Outline each uninfected red blood cell.
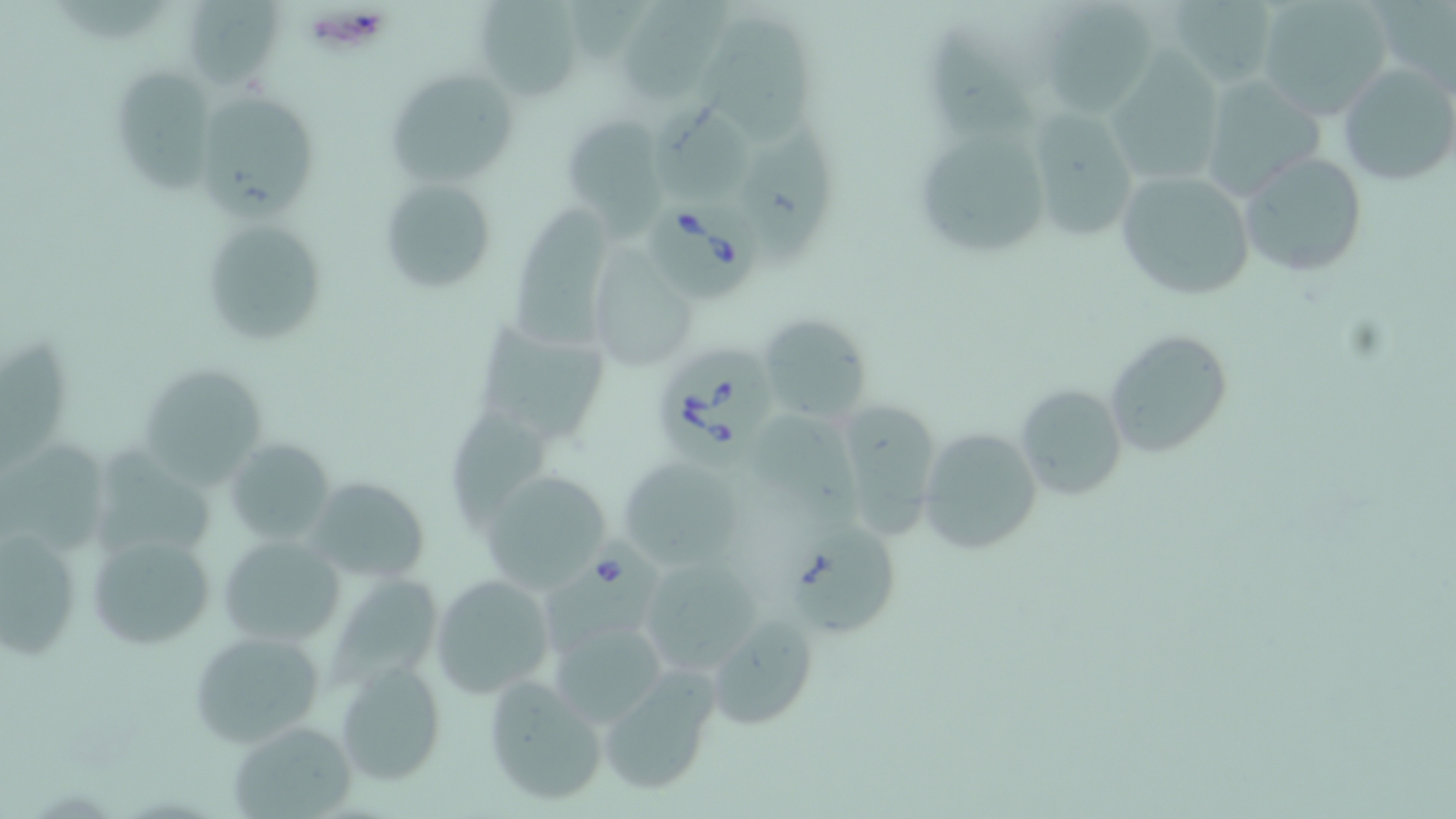

Approximate bounding boxes as named x1/y1/x2/y2 corners in pixels.
Uninfected red blood cells: (x1=54, y1=0, x2=173, y2=47), (x1=179, y1=0, x2=286, y2=91), (x1=474, y1=0, x2=585, y2=99), (x1=1162, y1=0, x2=1282, y2=90), (x1=1253, y1=0, x2=1397, y2=119), (x1=1370, y1=0, x2=1456, y2=95), (x1=611, y1=1, x2=733, y2=104), (x1=1035, y1=6, x2=1158, y2=114), (x1=693, y1=14, x2=816, y2=150), (x1=928, y1=34, x2=1033, y2=139), (x1=1103, y1=60, x2=1227, y2=188), (x1=109, y1=63, x2=219, y2=192), (x1=1338, y1=64, x2=1455, y2=188), (x1=386, y1=67, x2=520, y2=191), (x1=1197, y1=75, x2=1325, y2=199), (x1=196, y1=91, x2=320, y2=219), (x1=649, y1=94, x2=759, y2=208), (x1=1023, y1=108, x2=1138, y2=241), (x1=560, y1=114, x2=664, y2=221), (x1=923, y1=124, x2=1056, y2=253), (x1=736, y1=127, x2=840, y2=270), (x1=1237, y1=152, x2=1368, y2=277), (x1=1115, y1=169, x2=1257, y2=303), (x1=377, y1=176, x2=499, y2=294), (x1=509, y1=198, x2=624, y2=355), (x1=199, y1=215, x2=327, y2=345), (x1=587, y1=252, x2=697, y2=373), (x1=757, y1=313, x2=874, y2=422), (x1=473, y1=317, x2=612, y2=447), (x1=1104, y1=329, x2=1235, y2=459), (x1=1, y1=330, x2=75, y2=465), (x1=134, y1=363, x2=269, y2=488), (x1=1015, y1=384, x2=1128, y2=499), (x1=826, y1=399, x2=945, y2=538), (x1=449, y1=411, x2=555, y2=529), (x1=758, y1=413, x2=864, y2=528), (x1=917, y1=428, x2=1042, y2=555), (x1=225, y1=437, x2=336, y2=548), (x1=0, y1=439, x2=108, y2=567), (x1=88, y1=440, x2=223, y2=555), (x1=616, y1=455, x2=743, y2=568), (x1=477, y1=471, x2=615, y2=592), (x1=306, y1=475, x2=433, y2=583), (x1=788, y1=521, x2=899, y2=638), (x1=2, y1=529, x2=83, y2=662), (x1=85, y1=531, x2=219, y2=652), (x1=218, y1=534, x2=346, y2=648), (x1=636, y1=555, x2=770, y2=676), (x1=431, y1=574, x2=554, y2=699), (x1=328, y1=580, x2=445, y2=696), (x1=708, y1=616, x2=821, y2=730), (x1=549, y1=619, x2=665, y2=728), (x1=187, y1=628, x2=327, y2=748), (x1=333, y1=658, x2=447, y2=785), (x1=597, y1=670, x2=721, y2=796), (x1=481, y1=674, x2=608, y2=807), (x1=227, y1=719, x2=360, y2=818).

Summary:
  - Babesia divergens-infected red blood cell locations: (x1=646, y1=197, x2=764, y2=307), (x1=653, y1=335, x2=776, y2=461), (x1=539, y1=535, x2=661, y2=655)
  - Platelet locations: (x1=309, y1=6, x2=387, y2=53)
  - Slide-level diagnosis: Babesia divergens
  - Magnification: 1000x
  - Modality: optical microscopy
  - Field of view: single
  - Stain: May-Grünwald-Giemsa
  - Preparation: thin blood smear
  - Image size: 1456×819 pixels